Give the extent of all Plasmodium ovale-infected red blood cells.
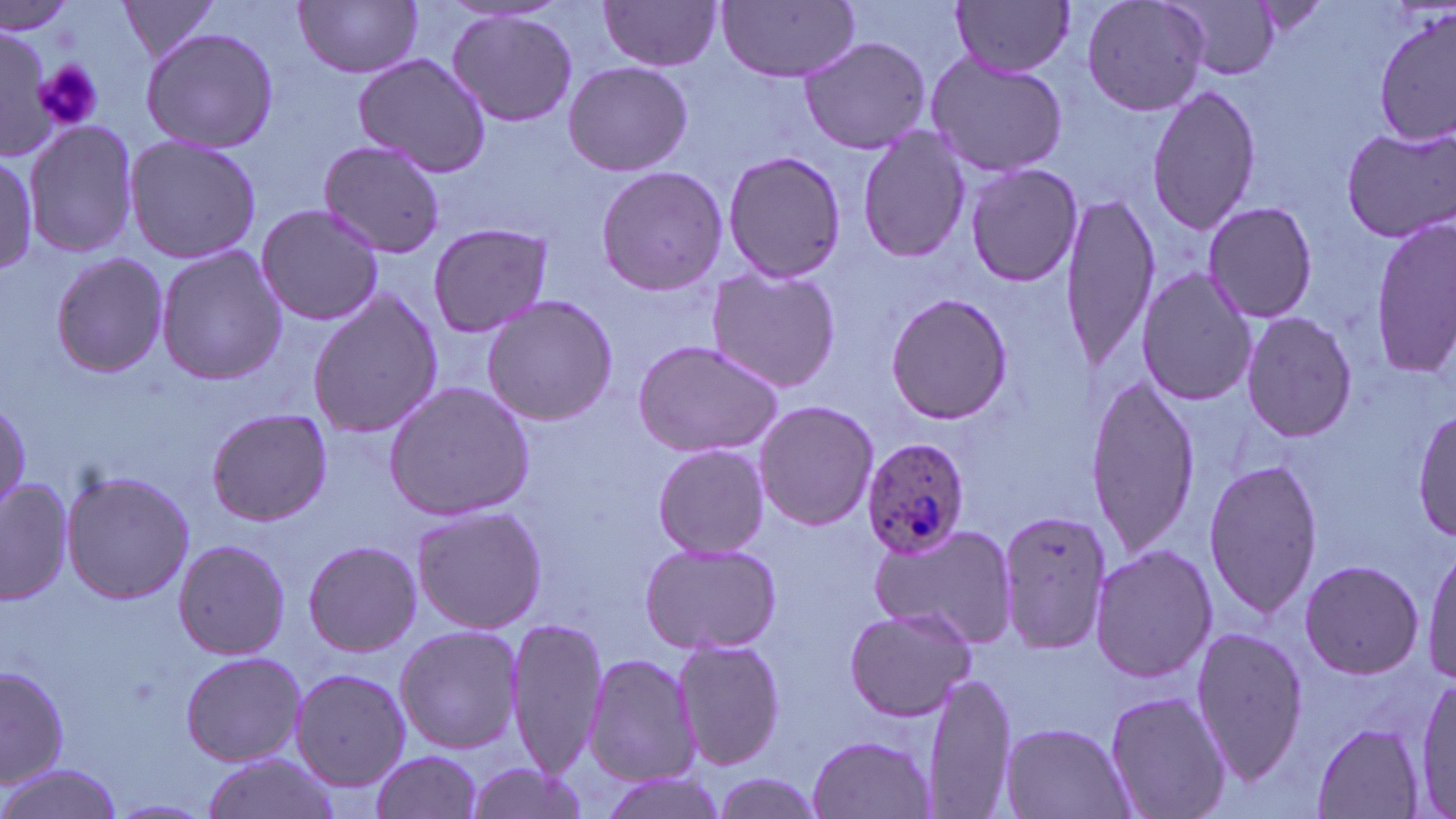

Approximate bounding boxes as (x1,y1)-(x2,y2) corner pairs in pixels.
Plasmodium ovale-infected red blood cells: (861,436)-(974,560).

Uninfected red blood cell locations: (950,0)-(1076,78), (1078,0)-(1211,118), (115,1)-(226,64), (294,1)-(425,80), (598,1)-(725,72), (717,1)-(861,82), (1163,1)-(1283,80), (447,9)-(579,128), (1375,10)-(1455,147), (140,26)-(279,155), (0,27)-(51,156), (799,34)-(930,156), (924,52)-(1069,177), (353,53)-(491,177), (563,60)-(695,177), (1145,84)-(1262,234), (25,121)-(139,260), (1339,123)-(1455,242), (855,127)-(971,265), (123,135)-(263,265), (318,138)-(447,260), (722,149)-(849,285), (0,153)-(37,274), (595,164)-(730,297), (965,164)-(1085,287), (1061,193)-(1159,371), (1201,202)-(1318,323), (255,203)-(384,327), (1369,214)-(1456,374), (425,222)-(556,340), (155,244)-(287,384), (51,251)-(169,378), (703,265)-(843,394), (1135,267)-(1257,407), (306,289)-(444,440), (884,293)-(1018,427), (481,294)-(621,427), (1240,311)-(1357,444), (631,339)-(785,458), (1082,373)-(1202,559), (382,380)-(535,523), (753,399)-(879,532), (0,400)-(32,511), (1413,407)-(1455,546), (206,408)-(332,526), (650,443)-(770,558), (1201,456)-(1322,620), (61,467)-(193,606), (0,478)-(75,605), (410,504)-(548,635), (996,508)-(1112,657), (864,522)-(1015,643), (172,539)-(289,660), (302,539)-(424,657), (638,540)-(782,654), (1423,541)-(1456,685), (1088,542)-(1217,685), (1298,558)-(1425,680), (842,605)-(980,722), (506,616)-(606,779), (393,623)-(523,755), (1188,625)-(1310,783), (673,637)-(789,772), (179,651)-(307,767), (585,651)-(697,786), (1,663)-(70,790), (289,667)-(410,791), (922,674)-(1017,819), (1411,676)-(1454,816), (1102,688)-(1232,819), (997,720)-(1135,819), (1311,721)-(1427,818), (806,732)-(938,819), (369,751)-(484,819), (199,753)-(340,819), (0,762)-(121,819), (462,762)-(591,819), (596,769)-(734,819), (710,771)-(830,817). Platelet locations: (34,59)-(102,130). Slide-level diagnosis: Plasmodium ovale. One field of a larger specimen. 1000x magnification. Image is 1456×819 pixels. May-Grünwald-Giemsa stain. Thin blood film. Light microscopy.